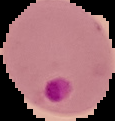
image type = segmented cell region with the area outside set to black
malaria status = parasitized
image size = 115×121 pixels
preparation = thin blood smear